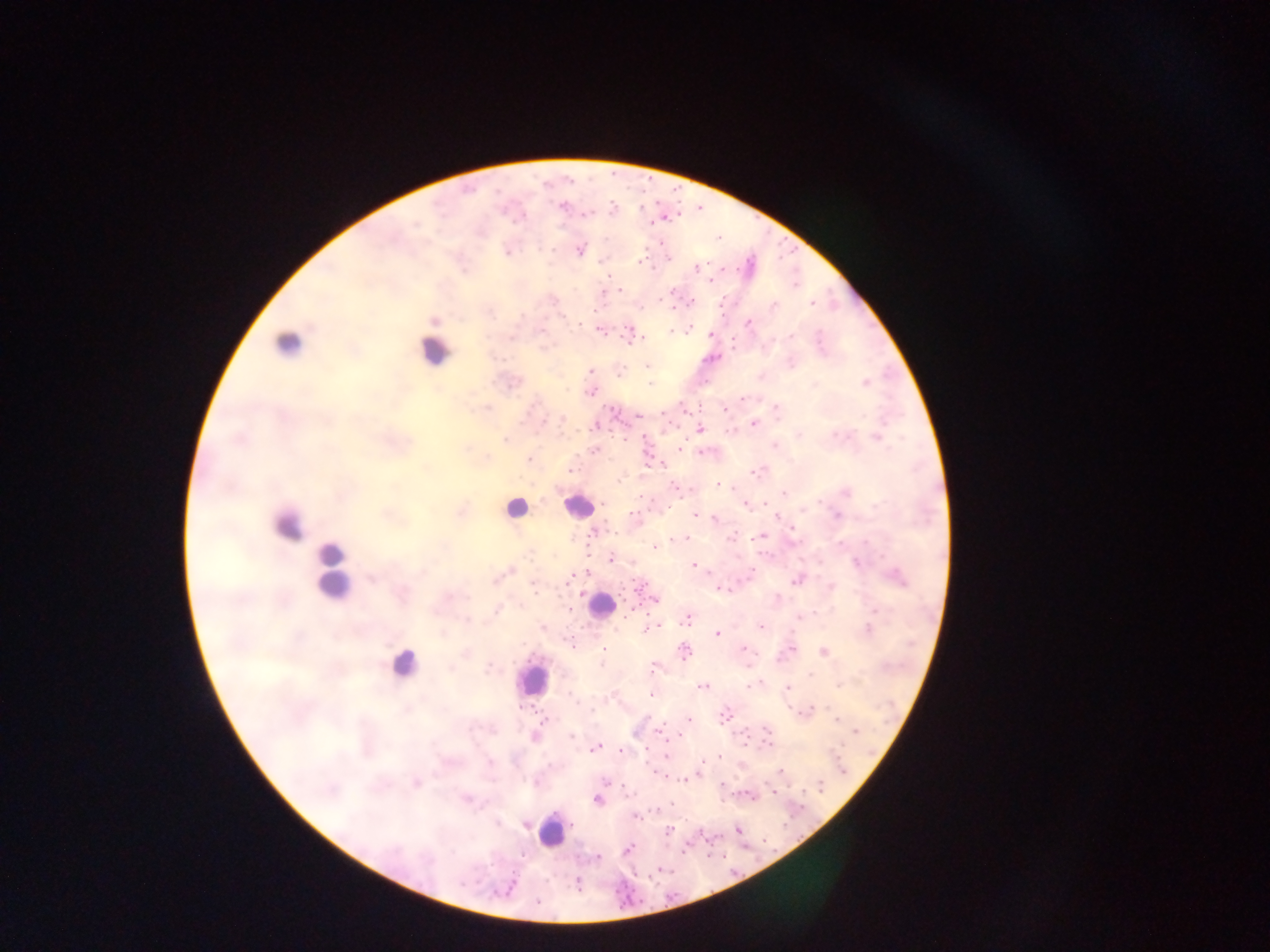 Approximate centers as {x, y} in pixels. Leukocyte locations: {284, 344}, {437, 354}, {579, 506}, {516, 515}, {285, 529}, {333, 554}, {332, 585}, {595, 605}, {405, 664}, {532, 678}, {551, 832}. Plasmodium parasite locations: {562, 206}, {611, 209}, {442, 212}, {586, 214}, {517, 219}, {417, 226}, {579, 249}, {507, 251}, {602, 259}, {639, 262}, {695, 269}, {607, 275}, {711, 279}, {674, 288}, {621, 290}, {604, 298}, {551, 299}, {689, 302}, {774, 306}, {812, 307}, {491, 312}, {433, 320}, {749, 322}, {689, 329}, {601, 330}, {788, 335}, {819, 335}, {510, 337}, {821, 337}, {735, 344}, {545, 346}, {646, 366}, {590, 369}, {620, 371}, {760, 377}, {864, 383}, {650, 384}, {814, 385}, {590, 390}, {743, 399}, {776, 408}, {486, 409}, {562, 420}, {754, 423}, {699, 429}, {731, 430}, {835, 433}, {799, 434}, {829, 435}, {876, 438}, {505, 439}, {500, 441}, {775, 446}, {679, 448}, {592, 449}, {464, 450}, {699, 451}, {485, 457}, {527, 458}, {425, 468}, {571, 470}, {761, 471}, {754, 472}, {619, 479}, {718, 485}, {396, 487}, {674, 488}, {846, 493}, {784, 494}, {744, 505}, {875, 505}, {820, 506}, {460, 511}, {693, 514}, {384, 515}, {713, 518}, {777, 518}, {593, 532}, {791, 533}, {763, 536}, {684, 537}, {679, 538}, {730, 538}, {867, 542}, {654, 546}, {527, 554}, {611, 559}, {691, 566}, {509, 569}, {585, 573}, {896, 574}, {371, 579}, {495, 580}, {568, 580}, {638, 581}, {795, 582}, {532, 586}, {831, 587}, {720, 589}, {580, 592}, {447, 597}, {654, 599}, {778, 599}, {630, 609}, {875, 610}, {496, 611}, {688, 618}, {799, 619}, {467, 620}, {667, 623}, {655, 626}, {761, 626}, {644, 629}, {868, 629}, {443, 631}, {716, 633}, {572, 642}, {791, 646}, {604, 648}, {743, 649}, {684, 652}, {466, 653}, {823, 654}, {780, 658}, {600, 662}, {450, 667}, {489, 667}, {652, 669}, {812, 675}, {809, 676}, {749, 685}, {839, 685}, {702, 686}, {786, 688}, {653, 695}, {812, 710}, {804, 711}, {723, 715}, {688, 718}, {545, 719}, {834, 719}, {472, 729}, {493, 732}, {660, 732}, {851, 732}, {667, 734}, {571, 735}, {472, 737}, {534, 737}, {768, 745}, {597, 746}, {664, 757}, {718, 758}, {488, 760}, {699, 770}, {780, 771}, {659, 773}, {435, 775}, {533, 782}, {608, 782}, {682, 782}, {416, 785}, {723, 787}, {770, 790}, {749, 796}, {466, 799}, {598, 801}, {668, 806}, {636, 817}, {637, 821}, {497, 822}, {527, 824}, {736, 830}, {669, 831}, {628, 848}, {596, 858}, {576, 884}, {536, 900}. Sample from Ghana. Mobile-phone photograph taken through the microscope. Single field of view. Thick blood smear. Image is 1270×952 pixels.